Identify the parasite.
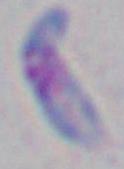

Toxoplasma gondii.

Captured at 1000x magnification. Photomicrograph.